Find the red blood cells and label each as P. falciparum-infected, uninfected, or of indeterminate infection status.
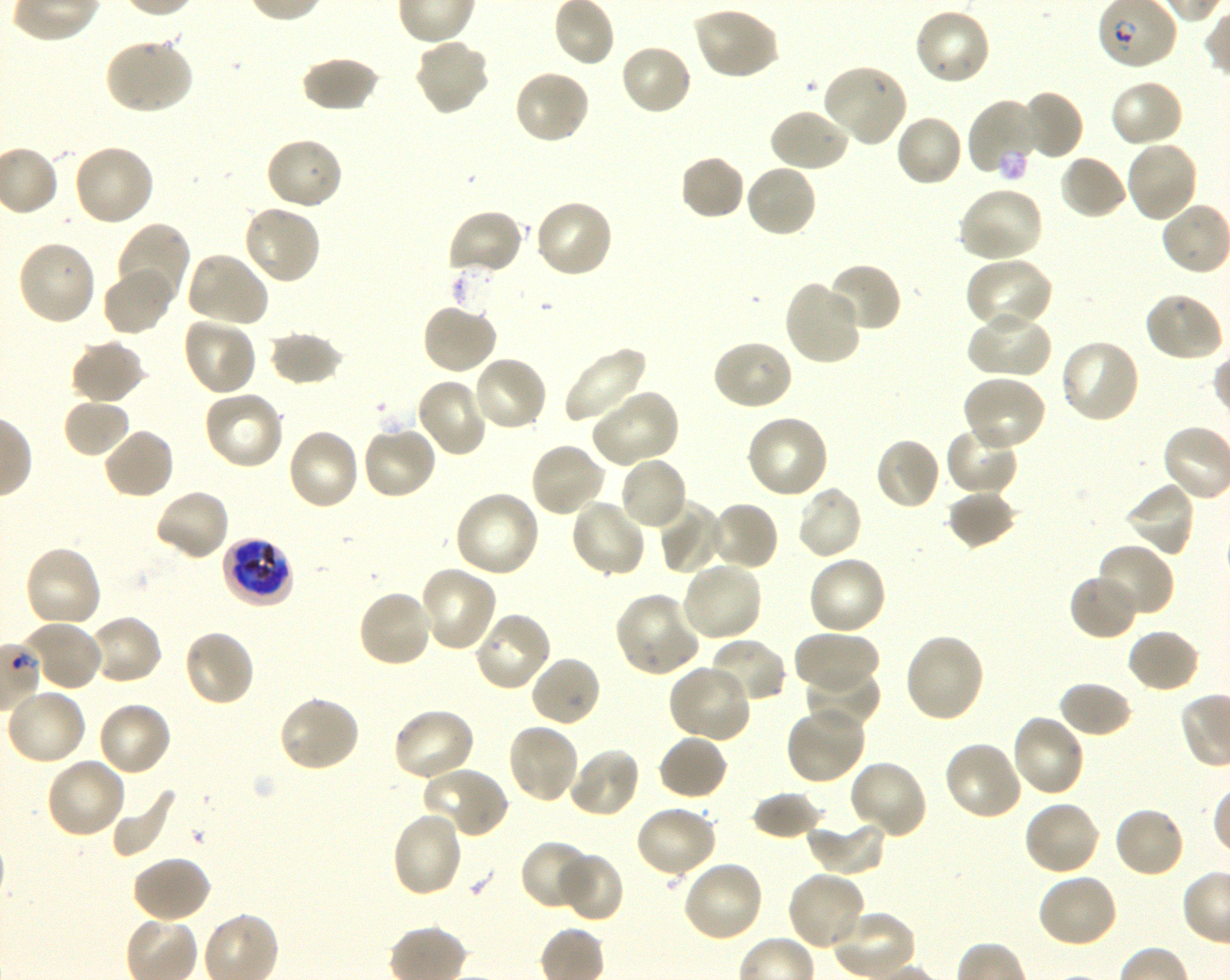
Approximate bounding boxes as (x1, y1, x2, y2) in pixels. Not every red blood cell is marked. A life-cycle stage — or a range of stages, where the recorded stages span more than one — follows each staged infected red blood cell.
Infected red blood cells: (221, 536, 296, 608) late trophozoite to late schizont.
Uninfected red blood cells: (692, 6, 780, 81), (913, 6, 992, 86), (104, 36, 194, 115), (413, 37, 492, 117), (619, 42, 693, 117), (301, 55, 380, 112), (821, 63, 908, 148), (513, 69, 591, 146), (1108, 78, 1185, 149), (1017, 90, 1083, 161), (967, 97, 1045, 179), (767, 106, 851, 173), (894, 114, 965, 188), (265, 135, 345, 211), (1123, 138, 1199, 223), (72, 143, 157, 227), (679, 153, 747, 221), (1058, 153, 1128, 220), (743, 162, 818, 239), (956, 185, 1045, 264), (532, 199, 614, 279), (242, 203, 322, 287), (446, 208, 525, 279), (115, 221, 191, 308), (16, 239, 97, 326), (184, 250, 270, 328), (964, 257, 1055, 333), (826, 263, 902, 334), (101, 266, 175, 337), (783, 279, 864, 366), (1142, 291, 1225, 363), (421, 302, 498, 376), (968, 308, 1053, 380), (182, 316, 257, 396), (268, 330, 345, 387), (69, 338, 146, 405), (711, 338, 793, 412), (1058, 338, 1142, 424), (561, 346, 648, 424), (471, 355, 548, 433), (960, 375, 1046, 455), (415, 376, 488, 456), (202, 389, 286, 471), (591, 389, 680, 467), (62, 397, 132, 459), (745, 413, 830, 499), (944, 422, 1019, 496), (361, 424, 437, 501), (101, 427, 176, 501), (286, 427, 361, 511), (874, 436, 942, 511), (528, 441, 607, 517), (618, 455, 689, 532), (1122, 480, 1196, 557), (795, 485, 864, 562), (153, 488, 231, 562), (946, 488, 1017, 549), (453, 490, 541, 579), (568, 497, 647, 579), (657, 500, 726, 574), (708, 500, 779, 571), (1095, 542, 1175, 620), (23, 544, 104, 629), (806, 554, 888, 636), (680, 560, 764, 644), (419, 565, 498, 653), (1068, 573, 1141, 642), (357, 589, 435, 669), (614, 591, 702, 677), (473, 610, 552, 692), (87, 614, 163, 687), (20, 620, 104, 692), (1125, 628, 1201, 694), (182, 629, 257, 709), (793, 629, 880, 693), (902, 632, 987, 724), (705, 637, 788, 705), (529, 653, 602, 728), (667, 663, 753, 743), (803, 663, 881, 730), (1057, 680, 1134, 739), (4, 687, 88, 767), (277, 694, 361, 773), (96, 701, 173, 779), (784, 705, 867, 786), (391, 707, 477, 783), (1010, 713, 1086, 798), (505, 722, 581, 806), (657, 734, 729, 802), (943, 739, 1024, 821), (567, 745, 642, 819), (44, 756, 127, 840), (849, 760, 928, 841), (421, 766, 510, 841), (111, 783, 177, 858), (750, 790, 824, 841), (1022, 798, 1102, 877), (633, 804, 718, 879), (1113, 805, 1186, 880), (390, 809, 465, 899), (807, 818, 887, 877), (518, 839, 596, 912), (556, 851, 625, 923), (131, 854, 212, 924), (679, 859, 764, 943), (786, 870, 868, 952), (1035, 872, 1120, 949), (831, 908, 916, 979).
No red blood cells of indeterminate infection status observed.

Blood group of the donor: O+. Giemsa stain. Single field of view. Thin blood film. 100x objective under oil immersion, numerical aperture 1.30. Image is 1230×980 pixels. Shaking in-vitro culture of P. falciparum strain 3D7.